Classify the preparation.
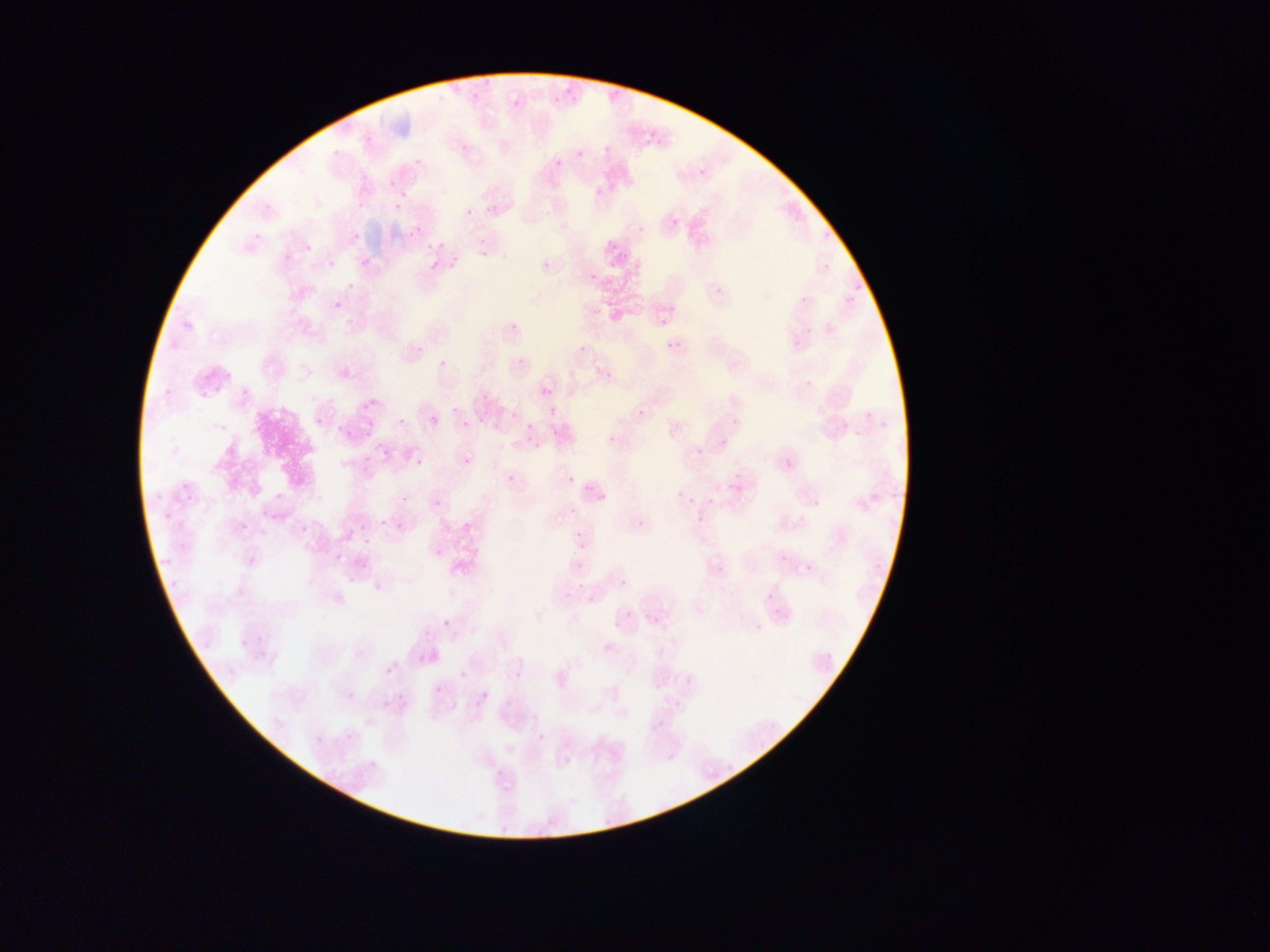

This is a thin smear.

field of view = single
country = Ghana
capture = mobile-phone photograph through a microscope
Plasmodium parasite locations = approximate bounding boxes as {left, top, right, bottom} in pixels: {551, 87, 573, 104}, {510, 98, 524, 111}, {566, 142, 584, 166}, {596, 142, 610, 156}, {547, 158, 564, 171}, {388, 178, 399, 192}, {589, 185, 607, 197}, {394, 201, 405, 212}, {465, 208, 474, 217}, {670, 216, 681, 229}, {411, 226, 422, 238}, {426, 238, 445, 254}, {304, 243, 313, 253}, {473, 252, 485, 260}, {359, 257, 371, 269}, {539, 258, 553, 273}, {328, 259, 336, 268}, {425, 259, 447, 273}, {430, 259, 441, 271}, {586, 271, 599, 284}, {333, 300, 342, 311}, {335, 301, 346, 313}, {655, 308, 673, 328}, {506, 319, 522, 336}, {576, 337, 592, 351}, {666, 338, 684, 356}, {516, 355, 527, 367}, {438, 357, 448, 369}, {196, 367, 214, 388}, {601, 367, 615, 382}, {801, 375, 818, 393}, {209, 382, 227, 396}, {541, 385, 553, 398}, {358, 399, 373, 409}, {635, 406, 648, 421}, {452, 407, 459, 415}, {510, 410, 518, 419}, {430, 416, 440, 427}, {314, 417, 324, 427}, {397, 417, 406, 427}, {460, 420, 469, 429}, {526, 423, 534, 433}, {330, 426, 347, 444}, {362, 429, 380, 446}, {606, 434, 618, 446}, {530, 440, 540, 449}, {695, 446, 706, 458}, {414, 456, 424, 468}, {462, 456, 473, 468}, {359, 465, 377, 479}, {507, 473, 516, 484}, {565, 475, 575, 486}, {675, 489, 685, 500}, {274, 491, 285, 502}, {432, 498, 443, 509}, {374, 516, 393, 537}, {350, 517, 368, 532}, {635, 517, 649, 532}, {396, 520, 407, 532}, {239, 521, 249, 532}, {568, 530, 583, 544}, {361, 538, 371, 548}, {433, 547, 446, 561}, {573, 552, 589, 578}, {334, 553, 344, 563}, {356, 558, 368, 570}, {573, 560, 586, 573}, {619, 578, 629, 589}, {763, 590, 778, 604}, {585, 592, 599, 607}, {625, 607, 639, 622}, {442, 618, 453, 631}, {649, 618, 663, 632}, {605, 621, 614, 633}, {254, 632, 266, 645}, {238, 635, 252, 651}, {385, 666, 395, 677}, {459, 670, 468, 680}, {650, 680, 667, 697}, {433, 685, 443, 695}, {347, 692, 356, 701}, {467, 695, 483, 709}, {343, 731, 358, 746}, {562, 756, 573, 768}
image size = 1270×952 pixels